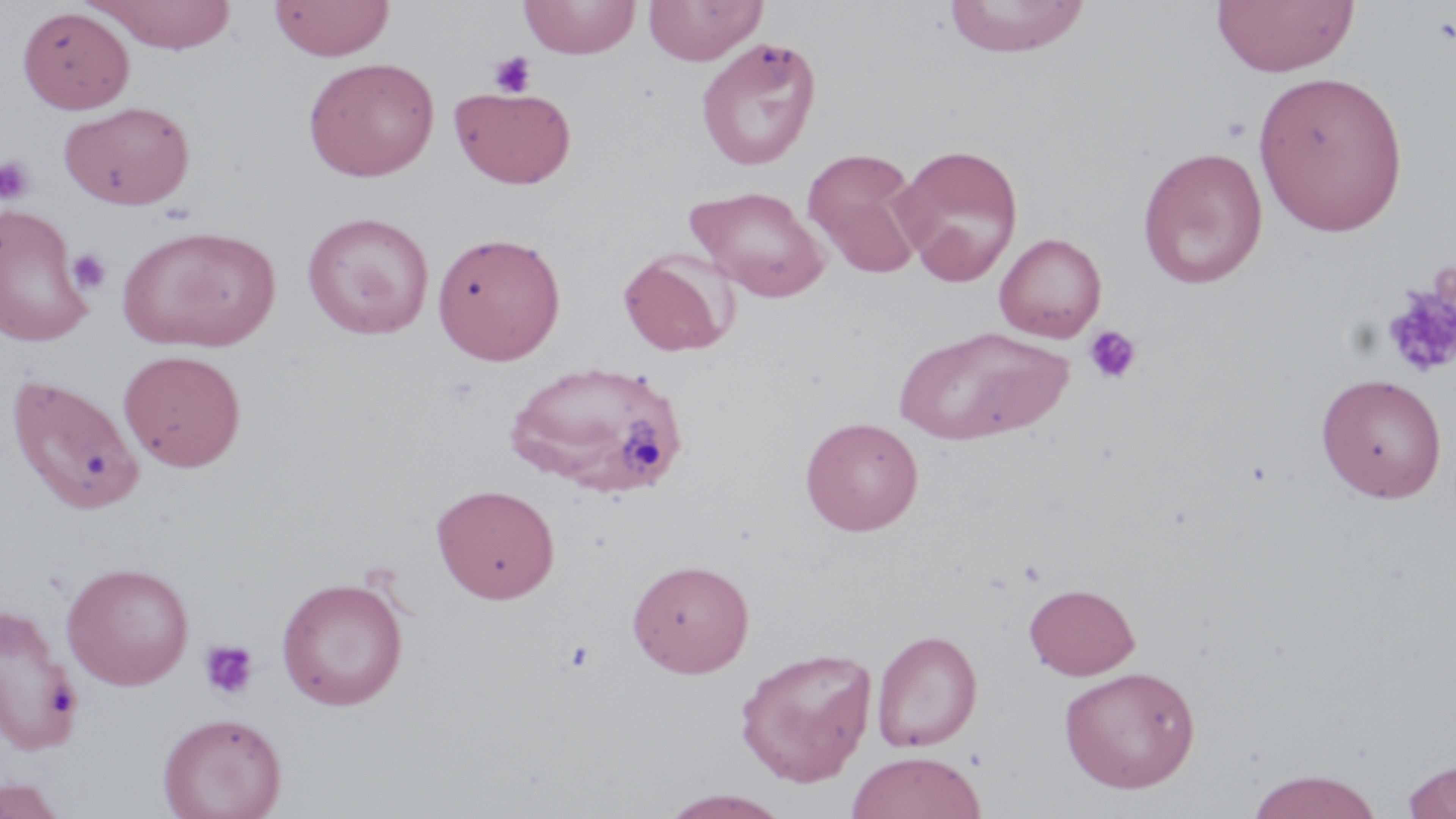

Summary:
  - Coordinate format: approximate bounding boxes as named x1/y1/x2/y2 corners in pixels
  - Uninfected red blood cell locations: (x1=91, y1=0, x2=238, y2=53), (x1=269, y1=0, x2=395, y2=61), (x1=519, y1=0, x2=641, y2=59), (x1=643, y1=0, x2=767, y2=66), (x1=942, y1=0, x2=1090, y2=57), (x1=1212, y1=0, x2=1358, y2=77), (x1=17, y1=6, x2=134, y2=113), (x1=695, y1=36, x2=822, y2=171), (x1=303, y1=57, x2=440, y2=181), (x1=1253, y1=69, x2=1409, y2=237), (x1=450, y1=85, x2=577, y2=189), (x1=59, y1=100, x2=195, y2=210), (x1=893, y1=142, x2=1024, y2=285), (x1=1137, y1=146, x2=1268, y2=289), (x1=802, y1=148, x2=926, y2=278), (x1=685, y1=185, x2=830, y2=302), (x1=0, y1=204, x2=94, y2=346), (x1=302, y1=211, x2=435, y2=339), (x1=118, y1=223, x2=280, y2=353), (x1=432, y1=231, x2=566, y2=365), (x1=995, y1=232, x2=1107, y2=342), (x1=617, y1=249, x2=738, y2=357), (x1=895, y1=326, x2=1070, y2=446), (x1=118, y1=350, x2=246, y2=471), (x1=506, y1=359, x2=688, y2=499), (x1=4, y1=372, x2=145, y2=514), (x1=1316, y1=373, x2=1448, y2=503), (x1=800, y1=416, x2=924, y2=536), (x1=432, y1=482, x2=560, y2=603), (x1=627, y1=558, x2=754, y2=677), (x1=61, y1=561, x2=195, y2=690), (x1=276, y1=576, x2=409, y2=710), (x1=1024, y1=582, x2=1140, y2=680), (x1=0, y1=604, x2=83, y2=755), (x1=871, y1=629, x2=983, y2=752), (x1=735, y1=646, x2=877, y2=786), (x1=1059, y1=665, x2=1201, y2=793), (x1=158, y1=712, x2=287, y2=819), (x1=845, y1=751, x2=987, y2=819), (x1=1400, y1=758, x2=1456, y2=818), (x1=1245, y1=769, x2=1385, y2=818), (x1=0, y1=775, x2=71, y2=819), (x1=657, y1=789, x2=793, y2=818)
  - Platelet locations: (x1=489, y1=51, x2=536, y2=97), (x1=1221, y1=116, x2=1253, y2=142), (x1=0, y1=155, x2=36, y2=204), (x1=67, y1=248, x2=112, y2=295), (x1=1383, y1=284, x2=1456, y2=378), (x1=1082, y1=324, x2=1142, y2=385), (x1=198, y1=639, x2=259, y2=701), (x1=561, y1=639, x2=596, y2=674)
  - Slide-level diagnosis: no evidence of blood parasites
  - Preparation: thin blood smear
  - Stain: May-Grünwald-Giemsa
  - Field of view: one of a larger specimen
  - Image size: 1456×819 pixels
  - Modality: optical microscopy
  - Magnification: 1000x